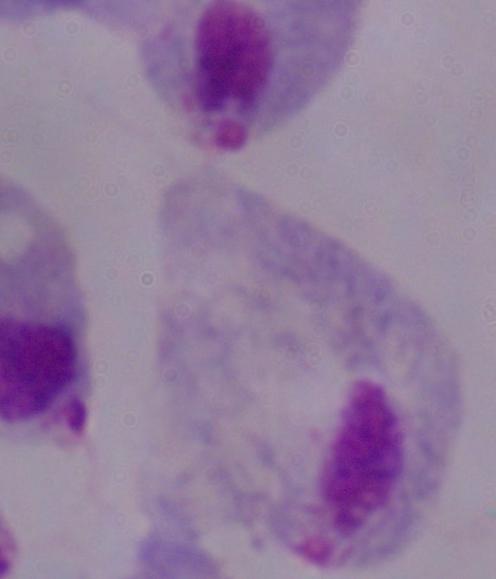
A trichomonad is shown. Photomicrograph. 1000x magnification.